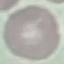

Malaria status: uninfected. Giemsa-stained preparation. Cell patch, automatically extracted from a larger field of view and resized to 64 × 64 pixels. Photographed with a smartphone camera at the microscope eyepiece. Thin blood film.